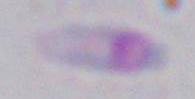

Summary:
  - Magnification: 1000x
  - Modality: micrograph
  - Identification: Toxoplasma gondii